State which parasite is depicted.
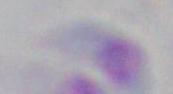

Toxoplasma gondii.

Summary:
  - Modality: photomicrograph
  - Magnification: 1000x